Comment on the morphology of the erythrocytes.
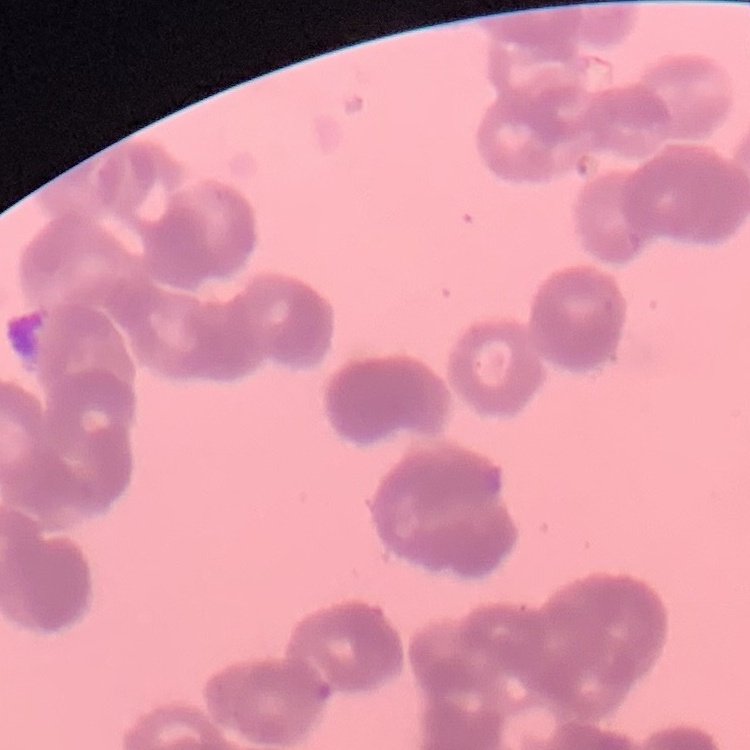
Rouleaux formation.

Square crop of a larger photomicrograph. Stained with either Field's or Giemsa. Thin blood film.